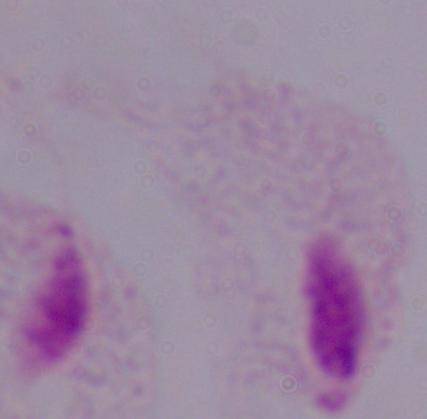
modality = photomicrograph
magnification = 1000x
identification = trichomonad